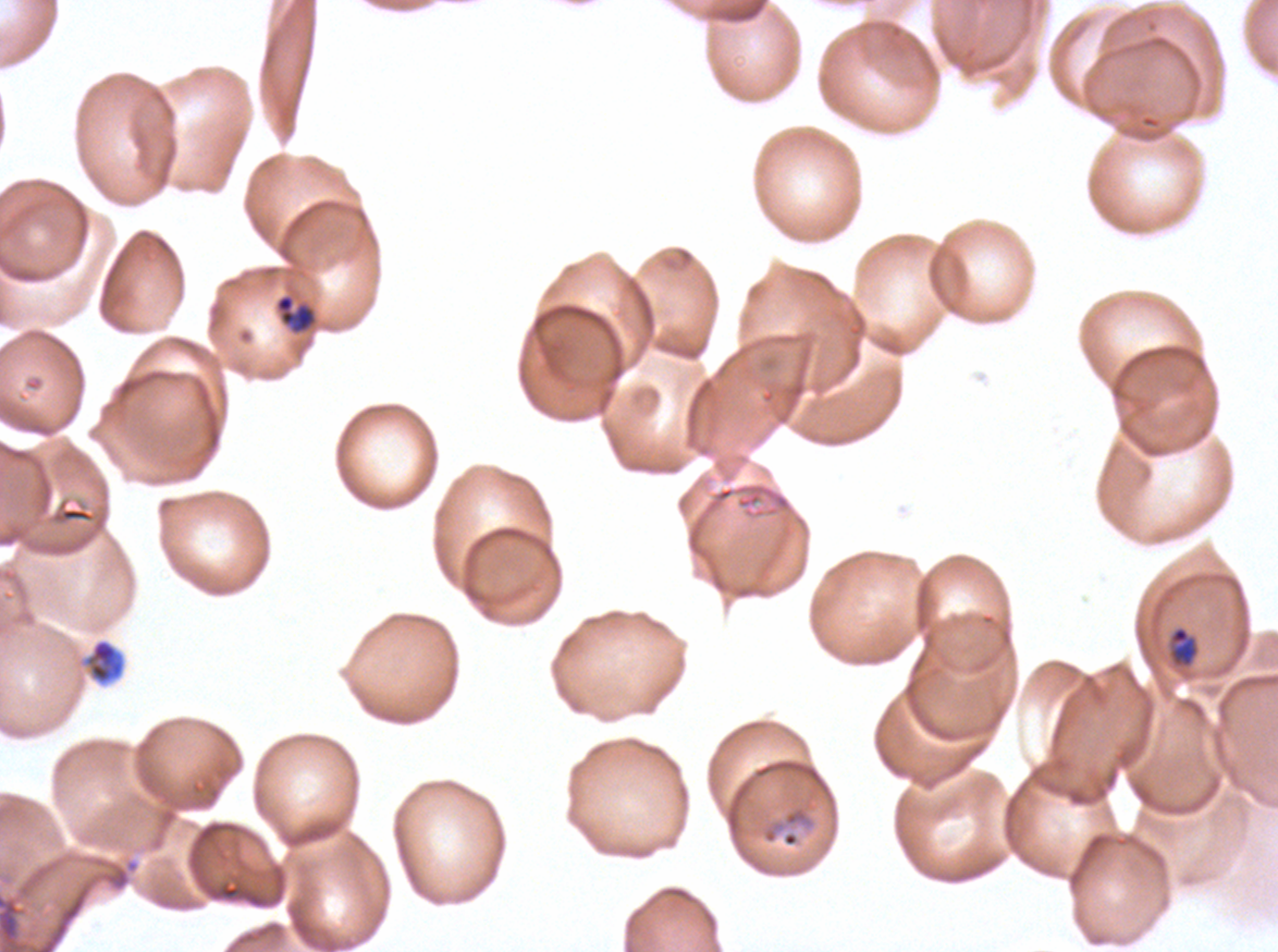 Approximate bounding boxes as [x1, y1, x2, y2] in pixels. Late-ring/early-trophozoite locations: [275, 294, 316, 334], [1170, 626, 1198, 666]. Ring locations: [783, 834, 797, 846]. Debris locations: [83, 638, 125, 685]. Giemsa stain. Ex-vivo Plasmodium falciparum culture from a patient in The Gambia, grown for 24 to 48 hours. Image is 1278×952 pixels. Thin blood smear. Life-cycle stages observed: ring, late-ring/early-trophozoite. A sub-image separated from a larger composite.